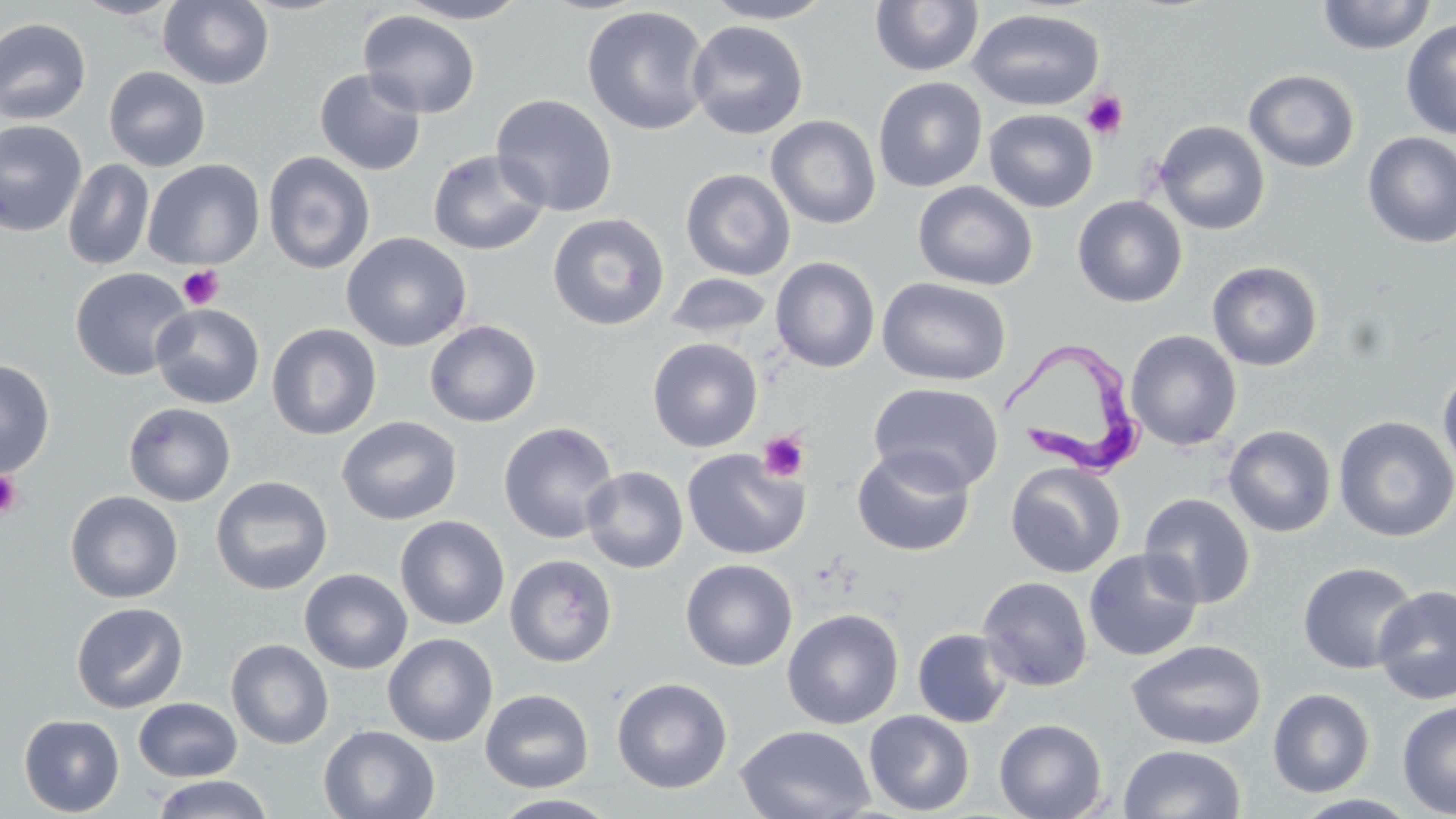
Trypanosoma brucei locations = approximate bounding boxes as (x1, y1, x2, y2) in pixels: (1000, 336, 1148, 479)
slide-level diagnosis = Trypanosoma brucei
image size = 1456×819 pixels
stain = May-Grünwald-Giemsa
field of view = single
preparation = thin blood film
uninfected red blood cell locations = approximate bounding boxes as (x1, y1, x2, y2) in pixels: (72, 0, 186, 20), (158, 0, 274, 89), (395, 0, 533, 24), (701, 0, 838, 24), (1315, 0, 1437, 55), (870, 1, 984, 76), (581, 5, 712, 136), (966, 8, 1104, 111), (357, 9, 481, 119), (0, 17, 92, 125), (1400, 18, 1455, 141), (686, 20, 809, 140), (103, 66, 211, 172), (314, 68, 427, 176), (1244, 69, 1360, 172), (873, 77, 988, 193), (491, 94, 618, 217), (983, 108, 1098, 213), (766, 115, 881, 230), (0, 119, 87, 236), (1152, 120, 1270, 236), (1361, 132, 1456, 249), (427, 149, 550, 256), (262, 151, 376, 274), (62, 159, 155, 272), (142, 159, 265, 270), (680, 168, 796, 280), (913, 181, 1039, 291), (1072, 196, 1188, 308), (547, 212, 670, 330), (341, 232, 472, 352), (770, 256, 881, 373), (1207, 260, 1323, 371), (69, 267, 193, 381), (663, 267, 880, 354), (665, 272, 775, 340), (877, 276, 1012, 386), (151, 303, 265, 409), (424, 320, 542, 427), (266, 323, 382, 440), (1125, 330, 1242, 451), (647, 337, 763, 452), (0, 358, 56, 478), (1437, 362, 1456, 483), (868, 382, 1004, 494), (123, 401, 236, 507), (336, 415, 462, 525), (1333, 415, 1456, 542), (498, 421, 619, 544), (1223, 424, 1337, 537), (852, 446, 976, 557), (682, 448, 809, 560), (1006, 460, 1126, 578), (581, 465, 688, 574), (1004, 474, 1256, 584), (210, 476, 333, 595), (64, 490, 183, 603), (1138, 493, 1256, 609), (395, 515, 510, 630), (1083, 549, 1204, 662), (505, 554, 617, 667), (680, 558, 798, 671), (1297, 561, 1420, 675), (299, 568, 413, 674), (976, 576, 1093, 691), (1372, 583, 1456, 705), (71, 601, 189, 714), (782, 608, 904, 729), (911, 628, 1013, 728), (383, 633, 499, 746), (226, 638, 334, 750), (1125, 639, 1267, 750), (612, 676, 733, 794), (480, 688, 594, 792), (1267, 688, 1376, 797), (132, 697, 242, 782), (1396, 700, 1456, 817), (864, 710, 975, 816), (19, 713, 125, 816), (994, 717, 1107, 819), (736, 724, 875, 819), (318, 725, 440, 818), (1118, 744, 1247, 818), (150, 774, 273, 819), (489, 793, 621, 818), (1291, 793, 1423, 818)
platelet locations = approximate bounding boxes as (x1, y1, x2, y2) in pixels: (1082, 90, 1129, 141), (177, 264, 224, 310), (756, 430, 810, 483), (0, 471, 25, 519)
magnification = 1000x
modality = optical microscopy